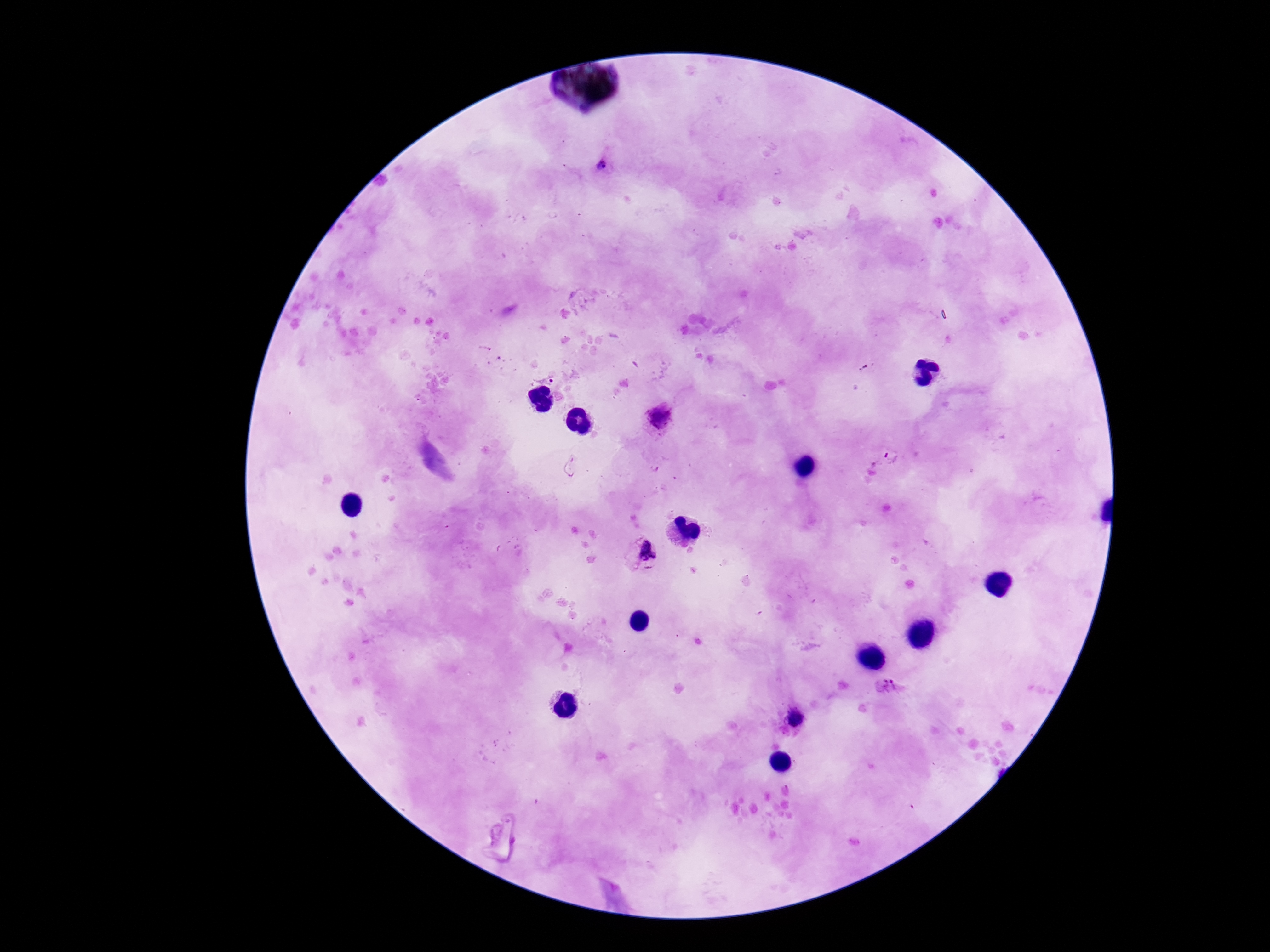
Approximate object centers, in pixels from the top-left corner.
Summary:
  - Plasmodium parasite locations: (x=603, y=166), (x=546, y=375), (x=659, y=417), (x=892, y=458), (x=643, y=554), (x=888, y=688), (x=794, y=718)
  - Patient malaria status: infected
  - Field of view: single
  - Image size: 1270×952 pixels
  - Capture: smartphone camera through the microscope eyepiece
  - Preparation: thick blood smear
  - Stain: Giemsa
  - Magnification: 100x